Report the malaria status of this cell.
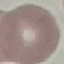

Uninfected.

Cell patch, automatically extracted from a larger field of view and resized to 64 × 64 pixels. Thin blood film. Giemsa stain. Photographed with a smartphone camera at the microscope eyepiece.